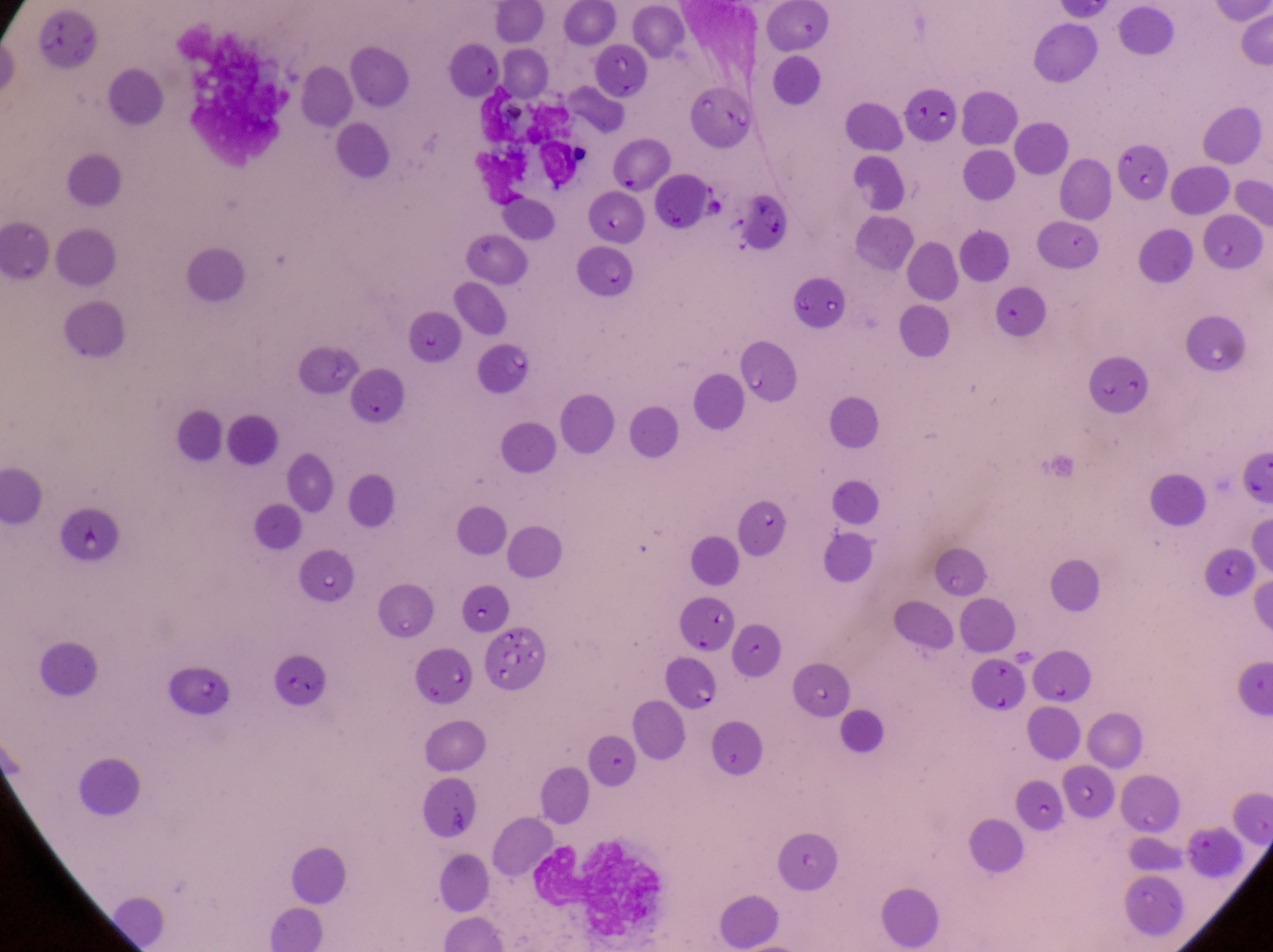 Approximate bounding boxes as {left, top, right, bottom} in pixels. Artifact (platelet-like body, stain precipitate, or debris) locations: {744, 192, 797, 247}, {486, 624, 553, 696}. Parasitised red blood cell locations: {481, 345, 536, 393}, {162, 661, 237, 718}, {669, 661, 726, 716}. Thin blood smear. At a magnification of 1000x. Captured by a smartphone held over the eyepiece of an Olympus CX-23 microscope. Single field of view. Image is 1273×952 pixels. Collected in Uganda.